Assess this cell for malaria.
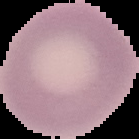

Uninfected.

image size = 139×139 pixels
image type = cell region segmented out of the field of view; surrounding area masked to black
preparation = thin blood film